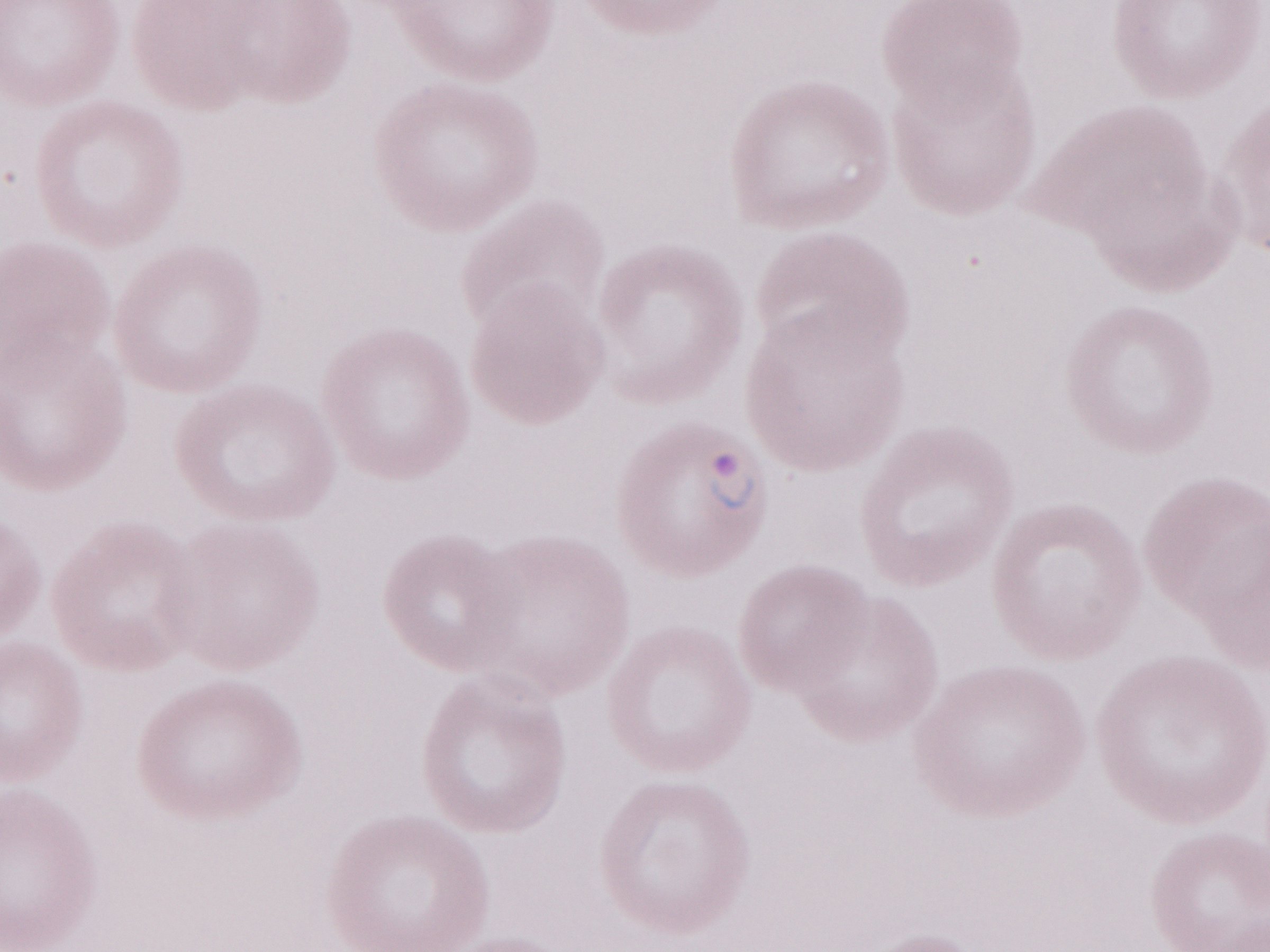
Image is 1270×952 pixels. Single field of view. Patient-level malaria diagnosis: positive. Olympus BX43 microscope, Olympus DP73 camera. May-Grünwald-Giemsa stain. 1,000x magnification. Thin blood smear.